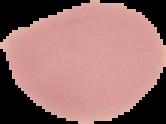 The area outside the segmented cell region is set to black. Result: negative for Plasmodium parasites. From a thin blood film. Image is 166×124 pixels.